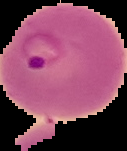 Malaria status: parasitized. Cell region segmented out of the field of view; the surrounding area is masked to black. Image is 127×151 pixels. From a thin blood smear.